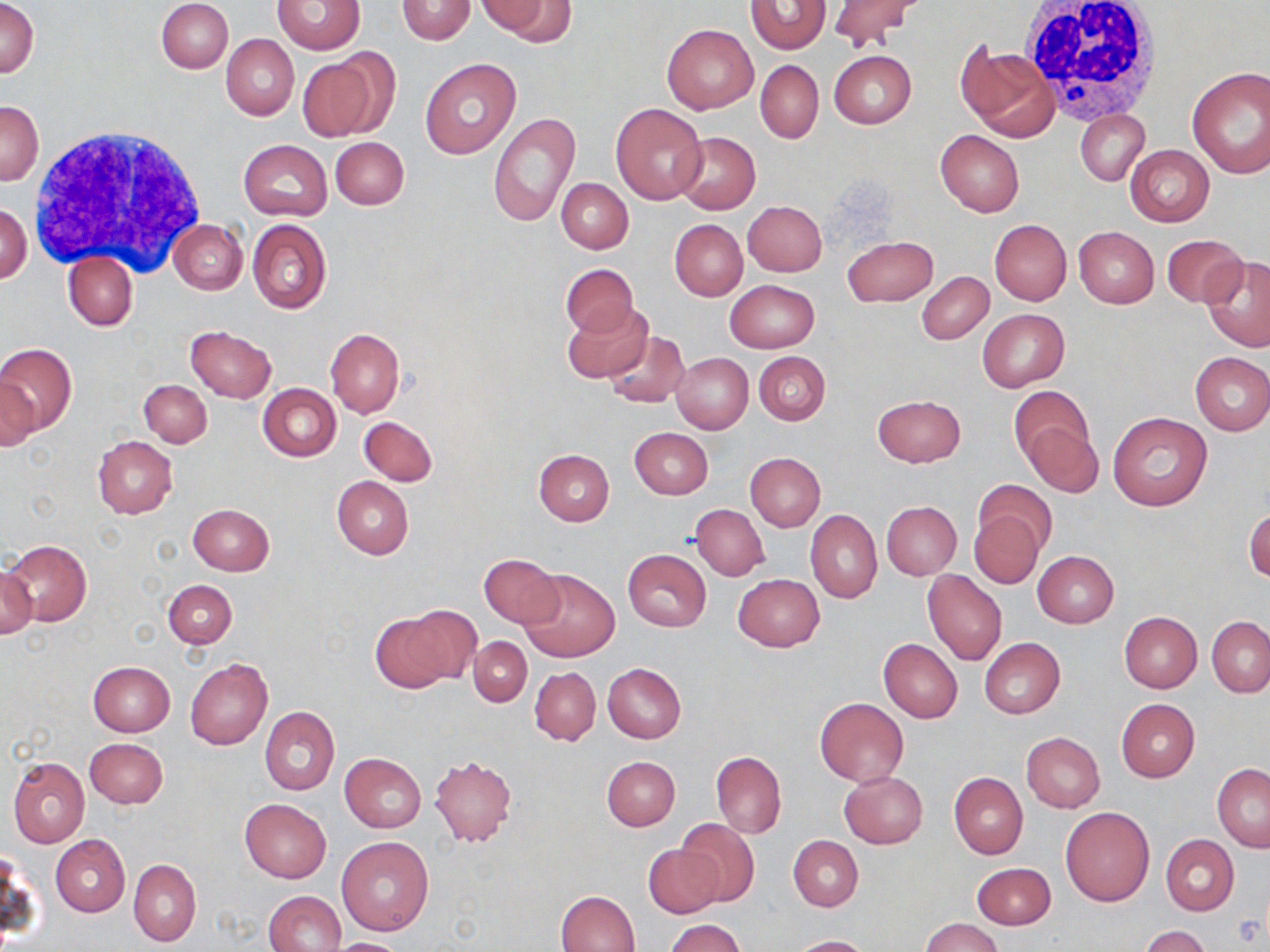

Summary:
  - Coordinate format: approximate bounding boxes as [x1, y1, x2, y2] in pixels
  - White blood cell locations: [1019, 2, 1164, 123], [27, 124, 209, 275]
  - Uninfected red blood cell locations: [2, 0, 39, 78], [156, 0, 232, 73], [396, 0, 476, 44], [479, 0, 572, 42], [273, 1, 365, 54], [745, 1, 830, 55], [828, 1, 920, 50], [662, 22, 758, 113], [221, 33, 299, 120], [957, 44, 1059, 142], [829, 51, 917, 129], [295, 54, 384, 141], [420, 58, 521, 158], [755, 60, 823, 143], [1186, 66, 1270, 178], [1, 99, 43, 186], [610, 103, 706, 204], [1076, 110, 1150, 185], [488, 111, 579, 228], [935, 130, 1025, 217], [676, 132, 760, 214], [330, 136, 408, 209], [238, 140, 332, 220], [1125, 145, 1214, 226], [557, 178, 634, 253], [1, 201, 31, 285], [742, 201, 827, 277], [170, 218, 248, 293], [247, 218, 331, 314], [670, 218, 748, 300], [989, 220, 1071, 305], [1074, 226, 1159, 307], [1162, 234, 1246, 308], [842, 235, 938, 308], [63, 252, 137, 331], [1200, 255, 1270, 352], [561, 263, 638, 337], [917, 272, 993, 344], [725, 280, 819, 352], [562, 303, 652, 383], [978, 309, 1069, 390], [186, 326, 276, 403], [326, 328, 405, 418], [603, 331, 690, 409], [0, 344, 74, 435], [754, 350, 830, 425], [671, 353, 752, 434], [1190, 353, 1270, 435], [1, 372, 39, 453], [139, 379, 211, 447], [257, 384, 340, 462], [1009, 387, 1093, 466], [873, 394, 965, 468], [1108, 411, 1212, 511], [1018, 414, 1103, 497], [360, 416, 437, 486], [630, 427, 713, 499], [92, 436, 177, 519], [534, 449, 615, 525], [745, 453, 825, 532], [331, 476, 414, 559], [975, 478, 1056, 552], [882, 501, 961, 579], [187, 503, 274, 575], [691, 504, 769, 581], [1244, 507, 1269, 583], [968, 509, 1045, 589], [805, 510, 882, 603], [2, 540, 91, 626], [623, 549, 711, 631], [1033, 550, 1119, 628], [479, 553, 565, 629], [1, 562, 38, 640], [518, 568, 620, 662], [922, 570, 1007, 665], [733, 573, 825, 652], [163, 579, 237, 649], [400, 605, 482, 686], [1119, 611, 1202, 693], [370, 614, 455, 693], [1207, 617, 1270, 697], [469, 636, 532, 706], [979, 637, 1065, 719], [878, 638, 963, 722], [185, 656, 272, 750], [88, 661, 175, 735], [603, 662, 686, 742], [530, 667, 600, 745], [814, 697, 908, 786], [1115, 698, 1201, 782], [259, 706, 338, 794], [1021, 733, 1105, 812], [84, 738, 167, 809], [711, 751, 786, 837], [339, 752, 426, 832], [429, 755, 517, 848], [602, 756, 679, 830], [8, 757, 89, 848], [1212, 762, 1270, 851], [839, 771, 928, 848], [949, 772, 1027, 858], [240, 798, 331, 882], [1060, 807, 1155, 907], [679, 819, 759, 905], [789, 835, 863, 911], [1161, 835, 1238, 915], [51, 836, 130, 917], [336, 836, 434, 935], [643, 844, 725, 919], [2, 853, 36, 945], [129, 859, 201, 947], [971, 862, 1056, 930], [262, 890, 345, 952], [555, 891, 641, 951], [920, 917, 1004, 952], [664, 919, 744, 952], [1141, 926, 1212, 952], [790, 935, 874, 952], [323, 938, 413, 952]
  - Slide-level diagnosis: no evidence of blood parasites
  - Field of view: single
  - Image size: 1270×952 pixels
  - Preparation: thin blood smear
  - Modality: optical microscopy
  - Stain: May-Grünwald-Giemsa
  - Magnification: 1000x